Identify the cell.
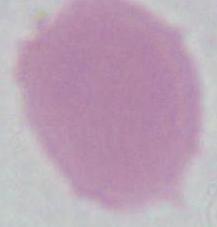
This is an erythrocyte.

Captured at 1000x magnification. Micrograph.